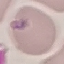

result = malaria parasites identified
capture = smartphone through the microscope eyepiece
image type = automatically extracted cell patch, resized to 64 × 64 pixels
stain = Giemsa
preparation = thin smear